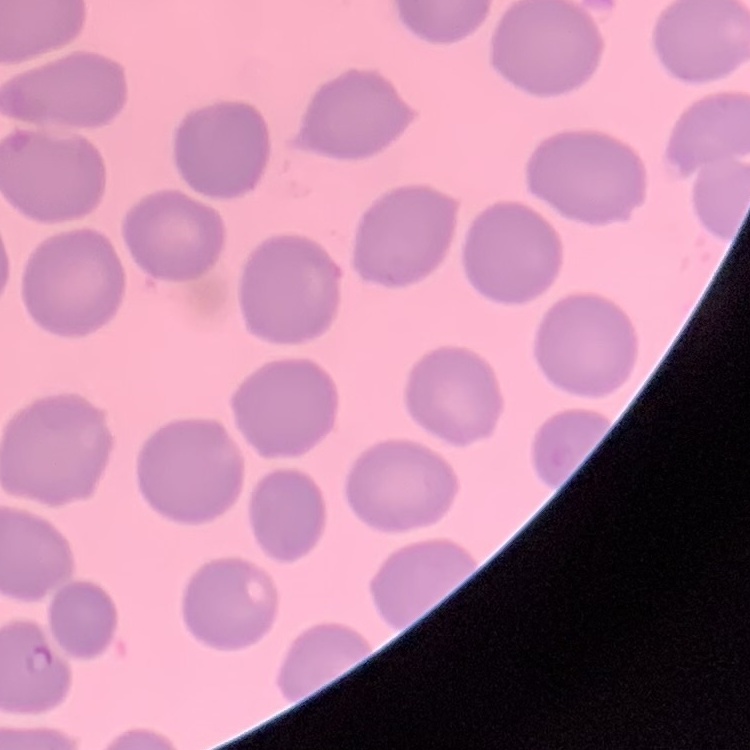
red blood cell morphology = no rouleaux formation
preparation = thin blood smear
stain = Field's or Giemsa
image type = one tile cut from a larger photomicrograph